Locate and identify every blood parasite.
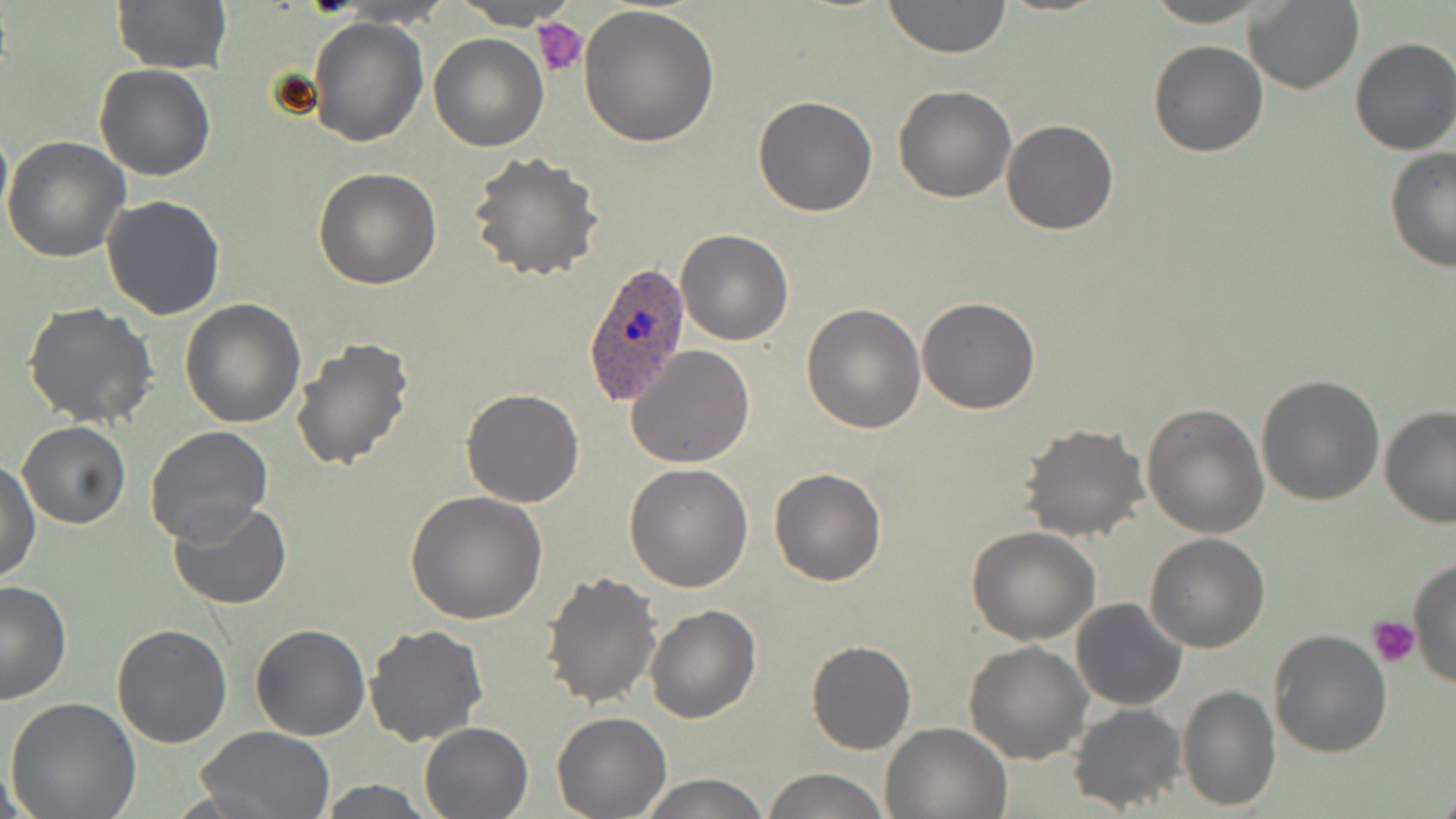
Approximate bounding boxes as named x1/y1/x2/y2 corners in pixels.
Plasmodium ovale-infected red blood cells: (x1=581, y1=261, x2=694, y2=406).
No Plasmodium falciparum, Plasmodium malariae, Plasmodium vivax, Babesia divergens, or Trypanosoma brucei observed.

Platelet locations: (x1=531, y1=18, x2=588, y2=78), (x1=1370, y1=616, x2=1420, y2=667). Uninfected red blood cell locations: (x1=109, y1=0, x2=231, y2=76), (x1=454, y1=0, x2=578, y2=29), (x1=881, y1=0, x2=1013, y2=57), (x1=1141, y1=0, x2=1279, y2=27), (x1=1244, y1=1, x2=1363, y2=95), (x1=577, y1=4, x2=720, y2=147), (x1=307, y1=18, x2=428, y2=147), (x1=429, y1=33, x2=547, y2=150), (x1=1349, y1=36, x2=1456, y2=156), (x1=1148, y1=39, x2=1269, y2=157), (x1=95, y1=65, x2=216, y2=182), (x1=893, y1=85, x2=1016, y2=203), (x1=752, y1=95, x2=879, y2=217), (x1=0, y1=114, x2=12, y2=233), (x1=1001, y1=120, x2=1118, y2=235), (x1=2, y1=136, x2=131, y2=263), (x1=1383, y1=147, x2=1456, y2=273), (x1=468, y1=151, x2=603, y2=282), (x1=313, y1=167, x2=441, y2=289), (x1=101, y1=194, x2=227, y2=320), (x1=675, y1=229, x2=793, y2=346), (x1=916, y1=296, x2=1039, y2=413), (x1=179, y1=298, x2=306, y2=428), (x1=23, y1=300, x2=162, y2=428), (x1=802, y1=302, x2=926, y2=434), (x1=290, y1=336, x2=417, y2=472), (x1=624, y1=344, x2=755, y2=467), (x1=1255, y1=373, x2=1386, y2=505), (x1=460, y1=388, x2=585, y2=508), (x1=1142, y1=401, x2=1270, y2=539), (x1=1379, y1=406, x2=1456, y2=528), (x1=17, y1=422, x2=130, y2=529), (x1=1017, y1=423, x2=1149, y2=542), (x1=145, y1=426, x2=273, y2=545), (x1=1, y1=462, x2=40, y2=584), (x1=623, y1=463, x2=753, y2=592), (x1=769, y1=467, x2=887, y2=587), (x1=403, y1=490, x2=549, y2=626), (x1=167, y1=499, x2=292, y2=610), (x1=967, y1=528, x2=1098, y2=645), (x1=1144, y1=533, x2=1271, y2=653), (x1=1410, y1=557, x2=1456, y2=692), (x1=540, y1=570, x2=662, y2=708), (x1=0, y1=581, x2=72, y2=705), (x1=1073, y1=598, x2=1188, y2=711), (x1=644, y1=605, x2=761, y2=724), (x1=250, y1=623, x2=370, y2=742), (x1=112, y1=625, x2=233, y2=748), (x1=365, y1=625, x2=490, y2=747), (x1=1269, y1=628, x2=1394, y2=758), (x1=805, y1=639, x2=916, y2=756), (x1=963, y1=641, x2=1094, y2=765), (x1=1177, y1=685, x2=1280, y2=810), (x1=4, y1=697, x2=142, y2=819), (x1=1068, y1=703, x2=1187, y2=815), (x1=551, y1=712, x2=671, y2=818), (x1=419, y1=721, x2=534, y2=818), (x1=880, y1=721, x2=1010, y2=818), (x1=193, y1=726, x2=338, y2=818), (x1=761, y1=768, x2=890, y2=819), (x1=635, y1=773, x2=772, y2=818), (x1=316, y1=779, x2=438, y2=817). Slide-level diagnosis: Plasmodium ovale. Thin blood film. Image is 1456×819 pixels. May-Grünwald-Giemsa stain. Captured at 1000x magnification. One field of a larger specimen. Light microscopy.